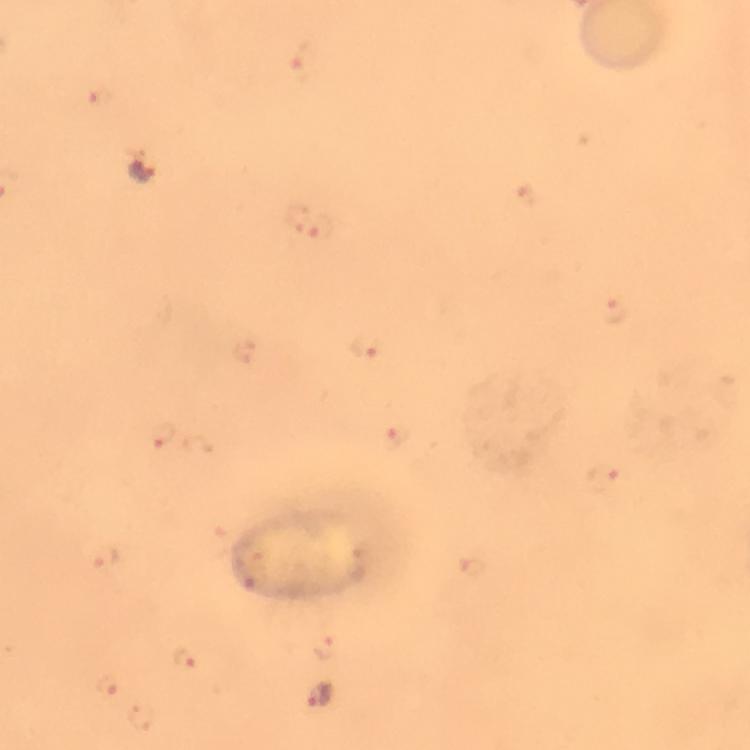 Approximate centers as (x, y) in pixels. Malaria parasite locations: (305, 64), (99, 98), (525, 195), (295, 219), (322, 227), (614, 312), (363, 347), (162, 435), (398, 437), (603, 479), (105, 558), (471, 566), (326, 647), (187, 659), (109, 687), (320, 695). Photographed with a smartphone mounted on the microscope. From a diagnostic examination for malaria. 100x magnification. Immersion oil applied. Giemsa stain. Thick blood film. Image is 750×750 pixels. Cropped region of a single field of view.